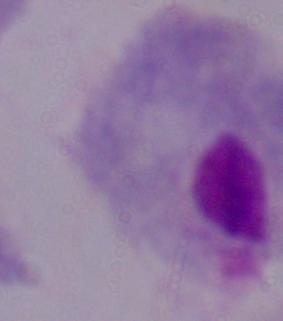

Summary:
  - Modality: micrograph
  - Identification: trichomonad
  - Magnification: 1000x